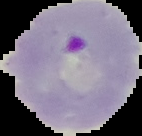
result = malaria parasites identified
preparation = thin blood film
image type = segmented cell region with the area outside set to black
image size = 142×136 pixels